Identify the blood parasite species.
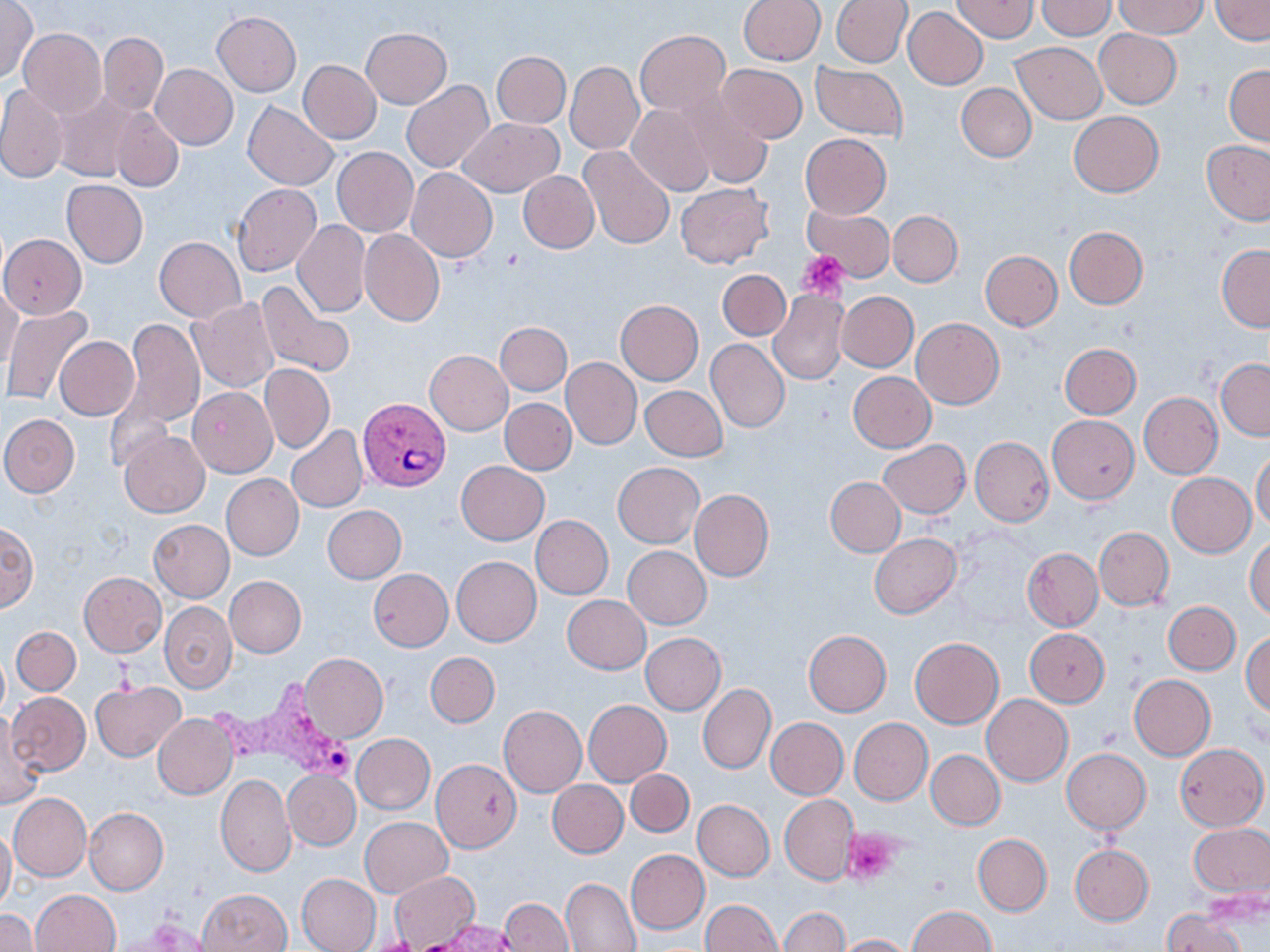

Plasmodium vivax.

Summary:
  - Coordinate format: approximate bounding boxes as (x1, y1, x2, y2) in pixels
  - Uninfected red blood cell locations: (737, 0, 825, 65), (832, 0, 911, 67), (951, 0, 1038, 42), (1037, 0, 1115, 40), (1111, 0, 1206, 39), (1209, 0, 1270, 43), (0, 1, 38, 81), (902, 7, 988, 90), (212, 12, 302, 96), (0, 14, 82, 103), (361, 27, 452, 108), (18, 28, 107, 118), (635, 29, 730, 116), (1095, 29, 1182, 109), (99, 32, 168, 114), (1010, 41, 1106, 124), (491, 51, 571, 128), (297, 59, 381, 144), (565, 62, 643, 154), (811, 63, 908, 139), (151, 64, 238, 150), (717, 64, 807, 143), (1225, 64, 1270, 145), (402, 80, 495, 174), (956, 83, 1036, 161), (0, 84, 69, 183), (50, 90, 142, 182), (676, 93, 774, 189), (244, 102, 338, 191), (627, 105, 716, 196), (110, 108, 183, 191), (1069, 111, 1163, 197), (457, 118, 563, 197), (800, 133, 890, 218), (1200, 140, 1270, 225), (579, 145, 675, 250), (332, 147, 419, 236), (407, 168, 497, 262), (519, 171, 599, 253), (61, 180, 148, 268), (231, 183, 322, 276), (676, 183, 773, 268), (803, 204, 894, 282), (887, 210, 963, 287), (292, 220, 369, 318), (1065, 226, 1147, 309), (359, 229, 445, 327), (3, 233, 86, 317), (154, 237, 245, 321), (1217, 244, 1270, 331), (980, 250, 1062, 330), (718, 269, 790, 341), (256, 281, 355, 380), (0, 284, 22, 374), (768, 289, 849, 385), (836, 291, 918, 372), (188, 298, 279, 392), (616, 300, 703, 384), (3, 307, 95, 407), (124, 318, 205, 428), (911, 318, 1003, 409), (496, 322, 571, 396), (55, 336, 140, 420), (706, 338, 789, 433), (1059, 343, 1141, 418), (424, 350, 513, 435), (560, 357, 641, 450), (1216, 359, 1270, 440), (260, 364, 335, 452), (848, 371, 935, 452), (640, 385, 727, 461), (189, 387, 277, 477), (1138, 392, 1222, 478), (499, 398, 576, 475), (1, 414, 79, 497), (1047, 415, 1139, 503), (287, 426, 368, 512), (118, 431, 210, 517), (970, 437, 1053, 525), (879, 439, 970, 519), (1251, 450, 1270, 533), (457, 461, 549, 544), (613, 462, 704, 548), (1166, 472, 1255, 557), (220, 473, 304, 560), (826, 477, 905, 556), (690, 490, 774, 581), (322, 504, 406, 583), (531, 515, 613, 598), (0, 519, 38, 611), (149, 519, 234, 602), (1093, 526, 1174, 610), (870, 533, 961, 617), (1245, 537, 1270, 619), (623, 546, 712, 628), (1023, 548, 1103, 630), (452, 557, 541, 646), (368, 569, 453, 651), (79, 572, 166, 656), (224, 575, 306, 657), (563, 595, 650, 674), (160, 601, 236, 691), (1163, 602, 1240, 675), (12, 626, 81, 695), (1026, 628, 1110, 706), (803, 630, 891, 715), (1242, 631, 1269, 718), (640, 632, 726, 714), (910, 636, 1003, 728), (0, 649, 10, 720), (300, 652, 389, 743), (425, 652, 500, 727), (1128, 674, 1215, 760), (89, 679, 184, 762), (698, 683, 775, 774), (7, 692, 90, 775), (983, 694, 1073, 786), (583, 699, 672, 786), (498, 705, 587, 796), (153, 713, 237, 799), (1, 716, 46, 812), (765, 718, 847, 799), (850, 719, 932, 804), (351, 733, 434, 814), (1174, 743, 1268, 830), (1061, 748, 1151, 832), (926, 750, 1004, 829), (431, 758, 521, 853), (284, 769, 360, 849), (626, 769, 694, 837), (215, 774, 297, 876), (548, 780, 628, 857), (9, 793, 92, 881), (780, 794, 860, 884), (693, 799, 774, 880), (84, 808, 168, 895), (360, 817, 453, 897), (1188, 822, 1270, 901), (0, 826, 15, 915), (973, 834, 1052, 916), (1070, 844, 1154, 926), (626, 849, 709, 934), (389, 872, 480, 948), (296, 873, 381, 952), (560, 877, 641, 952), (199, 889, 291, 952), (31, 890, 120, 952), (500, 898, 574, 951), (700, 900, 782, 952), (908, 905, 994, 952), (779, 906, 849, 952), (0, 909, 39, 951), (1163, 909, 1246, 952), (835, 933, 913, 951)
  - Platelet locations: (799, 251, 850, 301), (843, 827, 903, 886)
  - Plasmodium vivax-infected red blood cell locations: (357, 397, 452, 492), (210, 677, 359, 787)
  - Field of view: single
  - Image size: 1270×952 pixels
  - Preparation: thin blood smear
  - Stain: May-Grünwald-Giemsa
  - Modality: light microscopy
  - Magnification: 1000x